Assess for malaria.
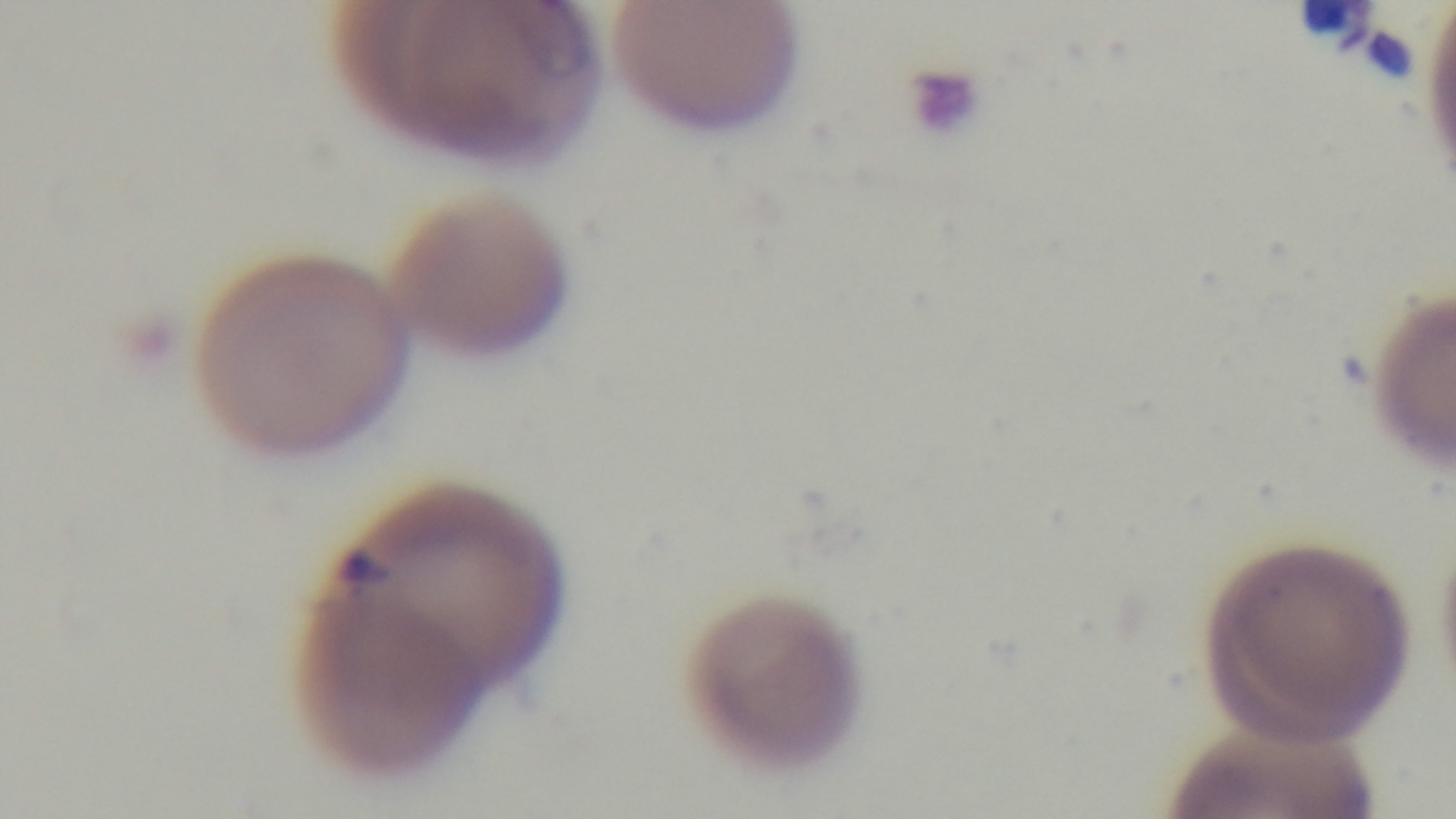

It is infected.

Photomicrograph. Preparation: thin blood film. 100x oil-immersion objective. Giemsa-stained. Mounted 4K digital camera. Single field of view.